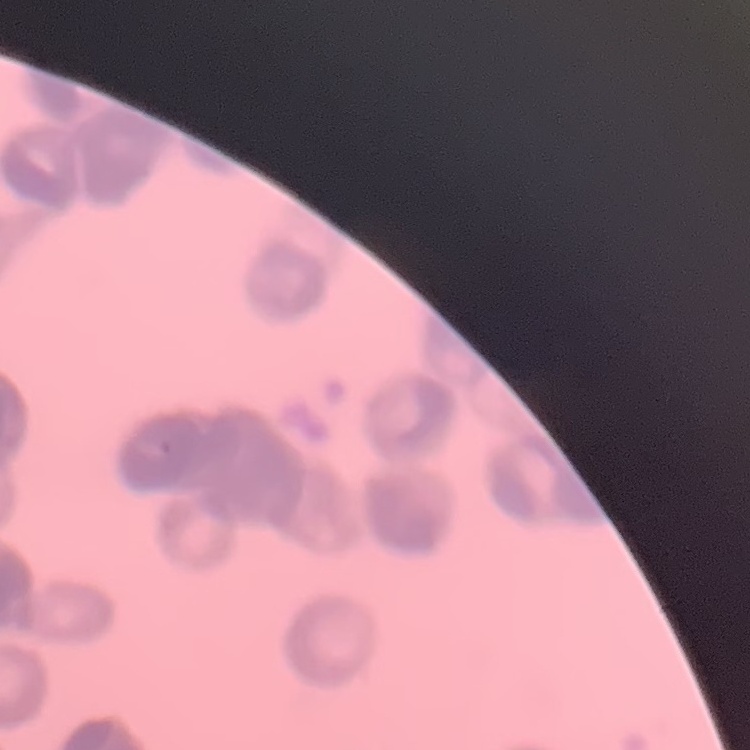
erythrocyte morphology = rouleaux formation
stain = Field's or Giemsa
preparation = thin peripheral smear
image type = square crop of a larger photomicrograph